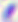
Summary:
  - Identification: Toxoplasma gondii
  - Magnification: 400x
  - Modality: photomicrograph